Locate every malaria parasite and every leukocyte.
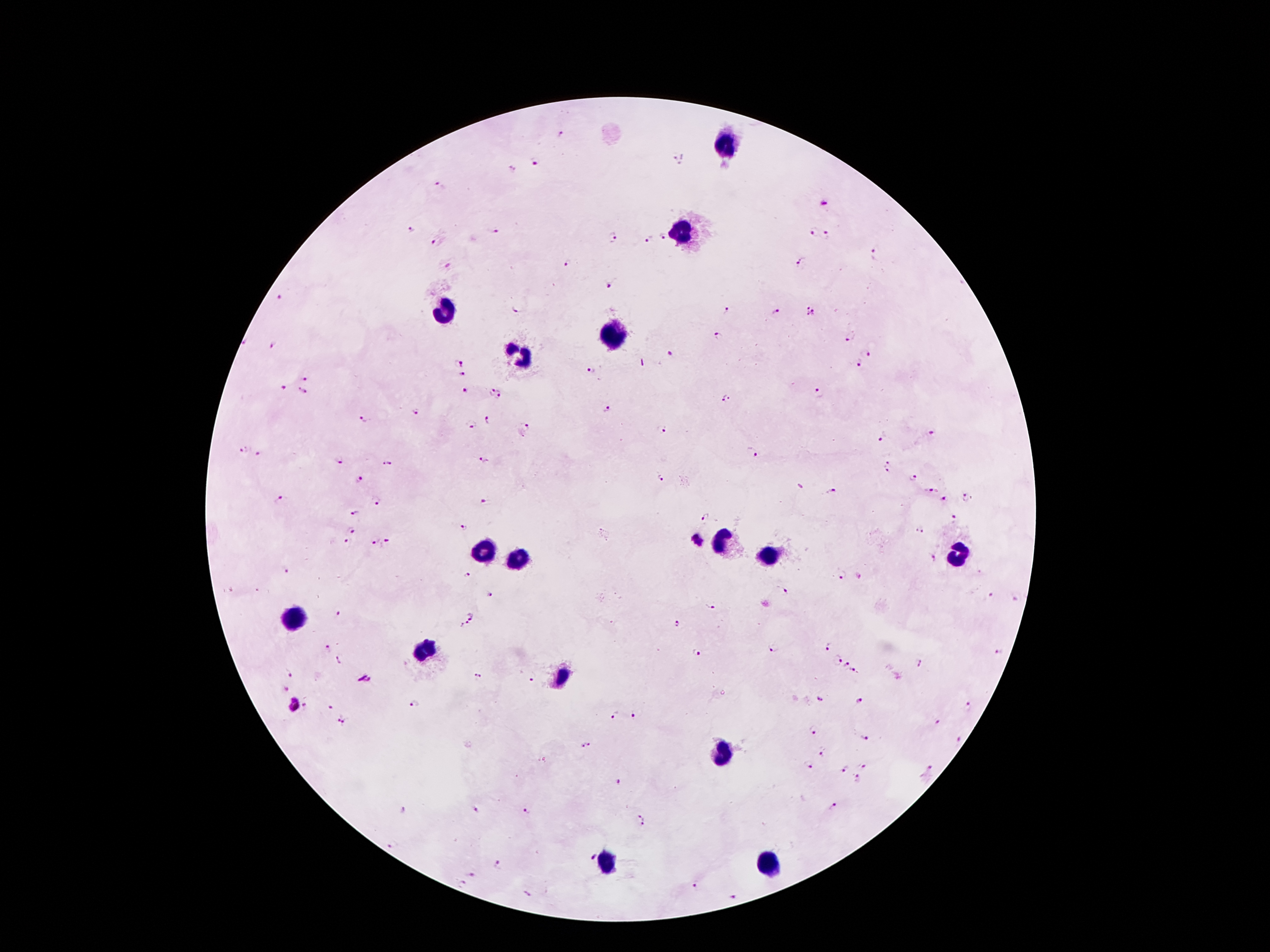

Approximate centers as (x, y) in pixels.
Malaria parasites: (561, 135), (673, 162), (535, 163), (511, 170), (438, 184), (825, 205), (409, 229), (494, 230), (814, 231), (828, 233), (613, 236), (664, 238), (650, 239), (436, 242), (873, 254), (568, 262), (799, 263), (448, 264), (607, 286), (282, 297), (517, 308), (727, 310), (778, 314), (811, 314), (720, 338), (849, 338), (242, 344), (273, 345), (867, 354), (672, 356), (458, 362), (857, 364), (591, 372), (463, 375), (305, 377), (281, 390), (490, 390), (466, 392), (301, 393), (818, 393), (500, 397), (726, 399), (607, 409), (415, 412), (363, 419), (488, 420), (471, 427), (526, 428), (661, 428), (931, 434), (883, 438), (242, 451), (751, 452), (259, 454), (482, 457), (337, 460), (385, 462), (887, 467), (661, 477), (914, 478), (359, 480), (929, 491), (833, 492), (968, 498), (944, 500), (279, 501), (375, 501), (484, 501), (355, 512), (705, 517), (954, 520), (349, 529), (463, 529), (920, 529), (698, 540), (373, 541), (345, 542), (387, 544), (932, 556), (283, 571), (467, 575), (841, 575), (859, 577), (784, 592), (490, 595), (992, 597), (1016, 600), (710, 607), (338, 613), (473, 615), (678, 624), (463, 625), (826, 646), (774, 647), (326, 649), (997, 652), (695, 654), (335, 661), (835, 661), (915, 663), (845, 666), (289, 670), (854, 670), (476, 677), (364, 679), (530, 682), (285, 688), (819, 700), (860, 701), (293, 705), (415, 705), (305, 707), (332, 707), (969, 708), (614, 714), (633, 714), (337, 718), (346, 722), (935, 723), (813, 731), (864, 738), (959, 742), (588, 744), (821, 752), (807, 766), (863, 766), (930, 767), (846, 769), (858, 780), (620, 781), (833, 806), (475, 810), (527, 810), (404, 812), (640, 821), (393, 847), (591, 856), (498, 863), (471, 874), (460, 884), (696, 885), (527, 894), (732, 896).
Leukocytes: (730, 146), (684, 232), (440, 311), (613, 332), (516, 357), (725, 540), (485, 548), (954, 553), (765, 556), (513, 558), (295, 617), (429, 647), (563, 678), (722, 756), (604, 861), (769, 864).

image size = 1270×952 pixels
field of view = one from this slide
stain = Giemsa
magnification = 100x
capture = smartphone through the microscope eyepiece
preparation = thick blood film
patient malaria status = infected with Plasmodium falciparum